Comment on the morphology of the red blood cells.
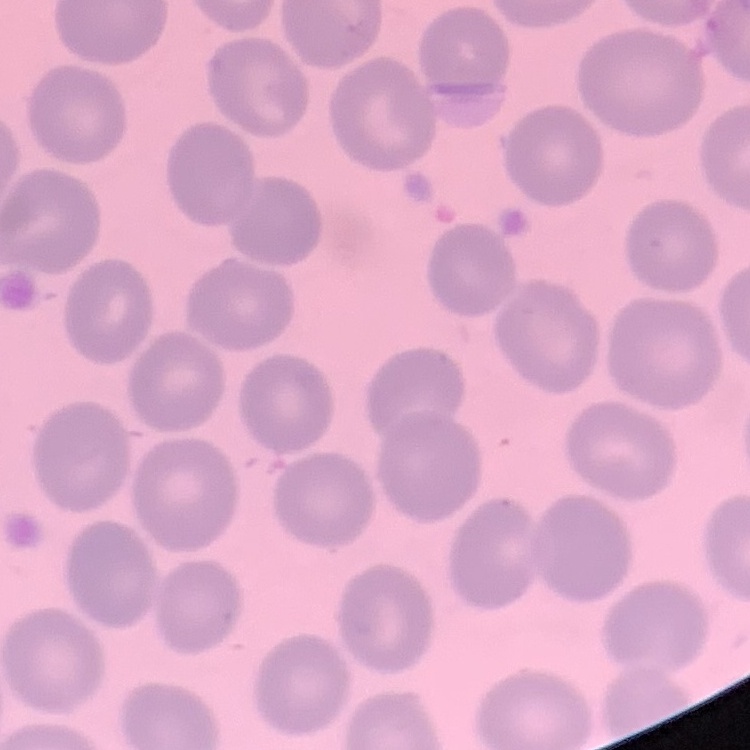
They show no rouleaux formation.

image type = square crop of a larger photomicrograph
preparation = thin blood film
stain = Field's or Giemsa